Classify this cell by malaria status.
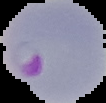

Parasitized.

preparation: thin blood smear
image_size: 106×103 pixels
image_type: segmented cell region with the area outside set to black